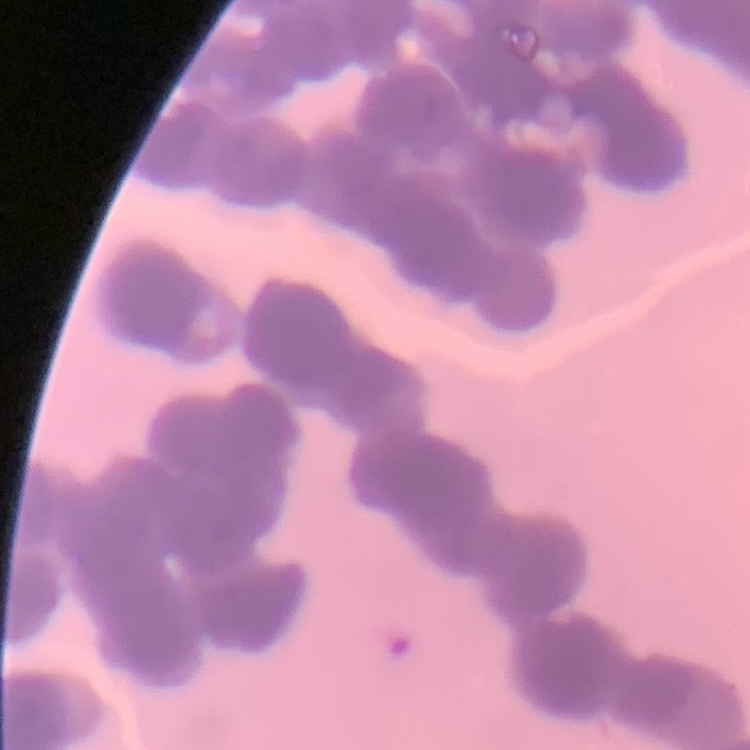

Summary:
  - Erythrocyte morphology: rouleaux formation
  - Image type: one tile cut from a larger photomicrograph
  - Stain: Field's or Giemsa
  - Preparation: thin blood film